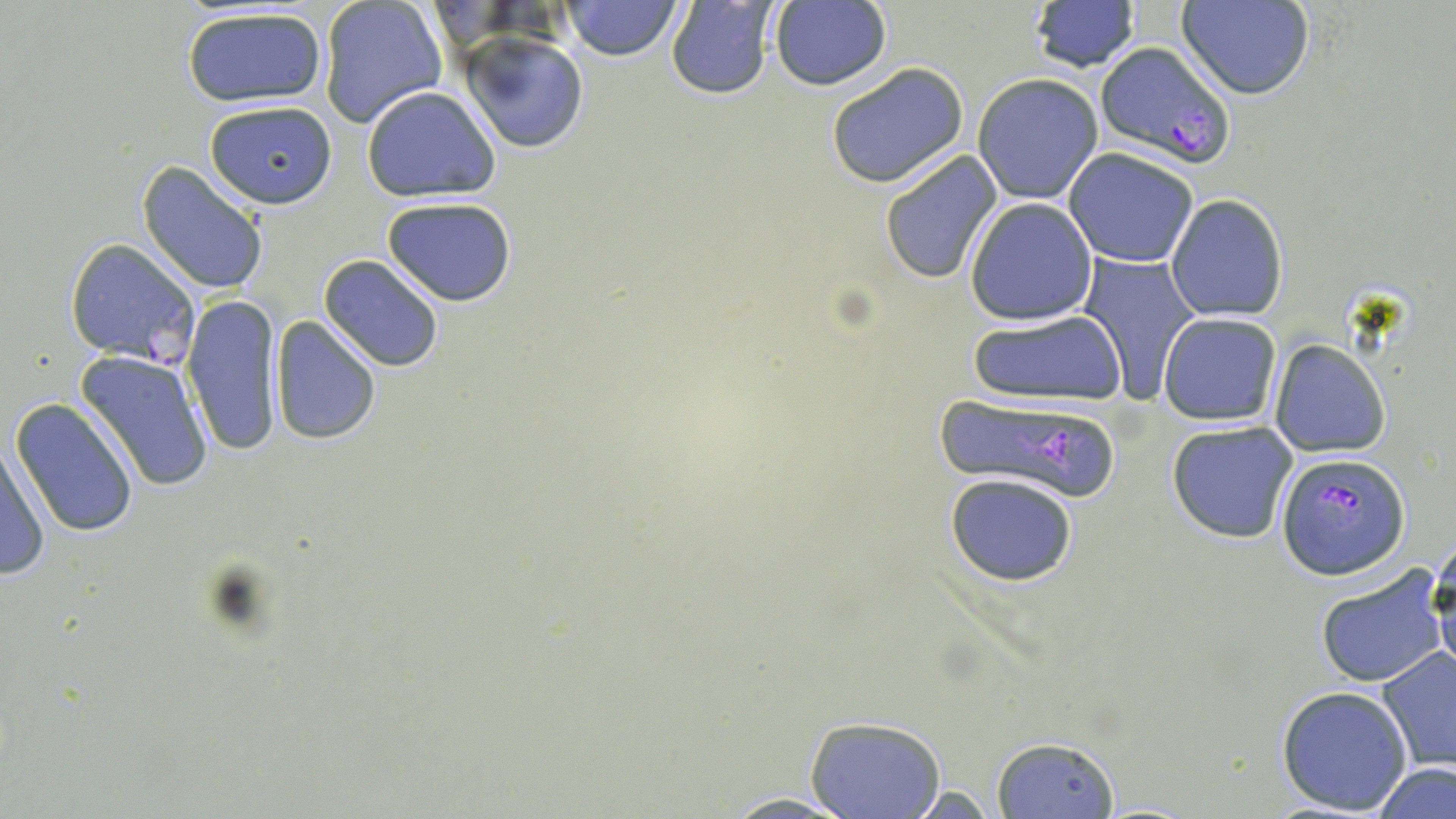
Summary:
  - Coordinate format: approximate bounding boxes as (x1,y1)-(x2,y2) corner pairs in pixels
  - Plasmodium falciparum-infected red blood cell locations: (1093,41)-(1237,167), (64,237)-(201,366), (932,393)-(1126,505), (1277,452)-(1409,580)
  - Uninfected red blood cell locations: (317,0)-(444,128), (562,0)-(684,60), (1178,0)-(1315,100), (768,1)-(892,92), (665,2)-(778,99), (1026,3)-(1142,75), (180,5)-(330,108), (461,33)-(586,152), (823,61)-(971,188), (973,74)-(1103,203), (361,86)-(501,201), (203,99)-(338,210), (1064,147)-(1199,268), (878,149)-(1004,285), (136,162)-(270,295), (1165,195)-(1288,322), (382,198)-(517,306), (963,199)-(1099,325), (1075,253)-(1201,402), (318,254)-(446,373), (182,291)-(285,457), (966,308)-(1127,410), (1157,313)-(1282,426), (269,315)-(380,444), (1271,340)-(1390,457), (72,348)-(215,492), (9,399)-(141,538), (1166,419)-(1299,544), (1,440)-(51,581), (944,472)-(1080,588), (1429,540)-(1456,682), (1314,563)-(1448,689), (1377,649)-(1456,771), (1276,684)-(1414,816), (803,715)-(949,819), (990,735)-(1122,819), (1373,761)-(1456,818), (712,792)-(867,817)
  - Slide-level diagnosis: Plasmodium falciparum
  - Field of view: one of a larger specimen
  - Stain: May-Grünwald-Giemsa
  - Magnification: 1000x
  - Preparation: thin blood smear
  - Image size: 1456×819 pixels
  - Modality: light microscopy